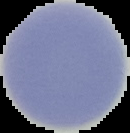
From a thin blood smear. Result: negative for malaria parasites. Cell region segmented out of the field of view; the surrounding area is masked to black. Image is 130×133 pixels.